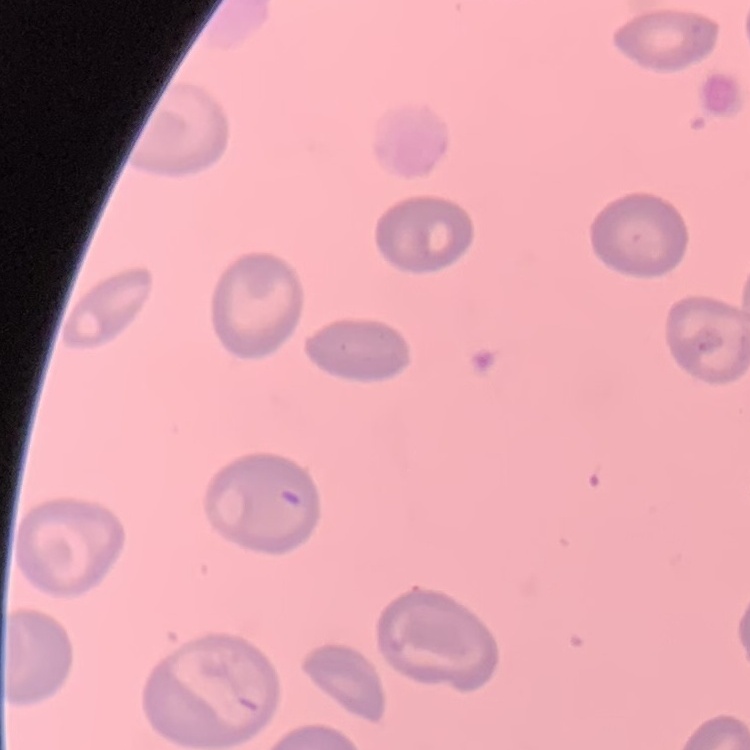
The red blood cells exhibit no rouleaux formation. One tile cut from a larger photomicrograph. Thin peripheral smear. Stained with either Field's or Giemsa.